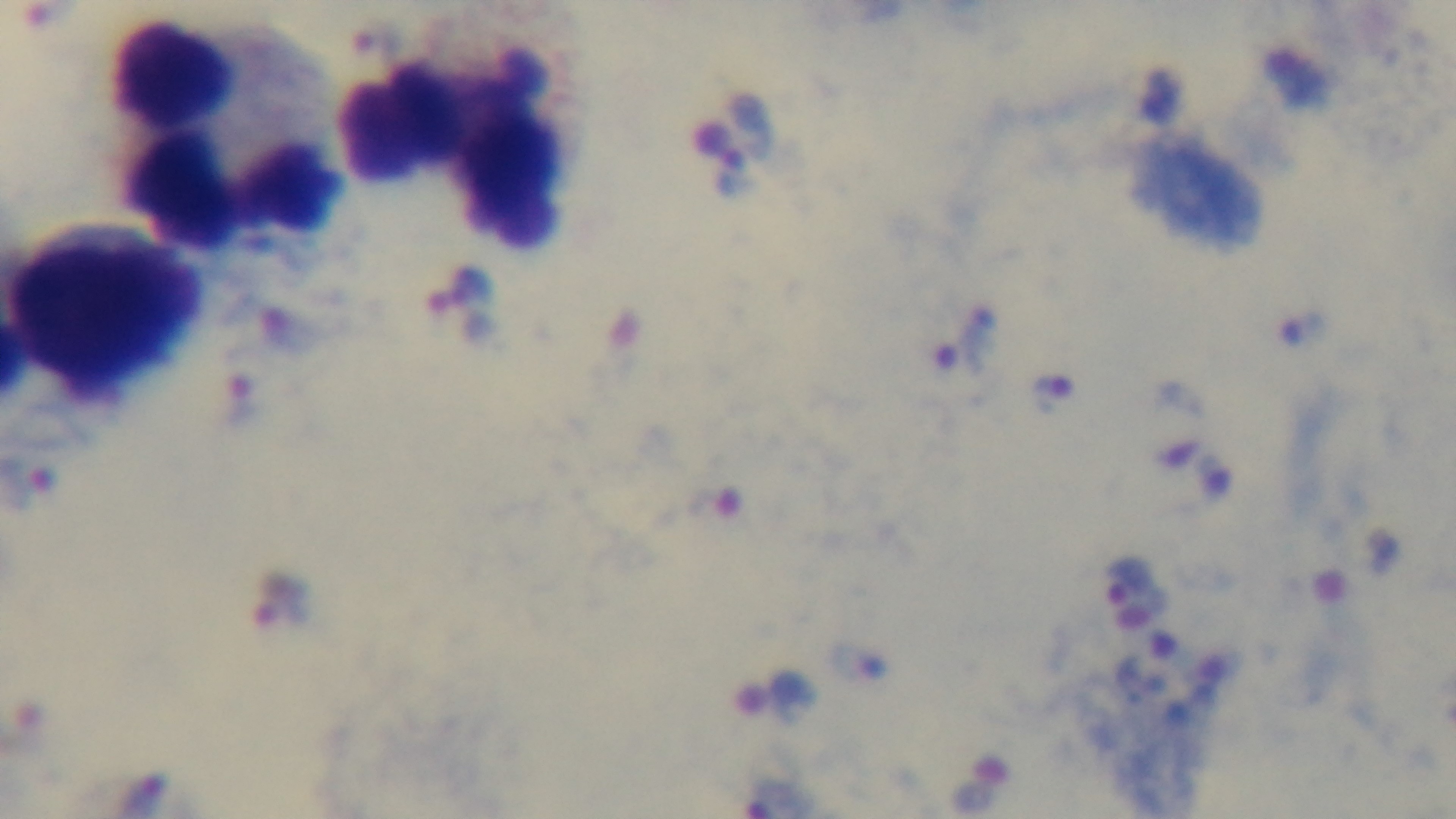
Malaria status: positive. Preparation: thick blood film. Mounted 4K digital camera. One field from the slide. Light microscopy. Giemsa stain. Oil-immersion objective, 100x.